Classify this cell by malaria status.
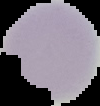
It is uninfected.

Image is 100×106 pixels. Cell region segmented out of the field of view; the surrounding area is masked to black. From a thin blood smear.